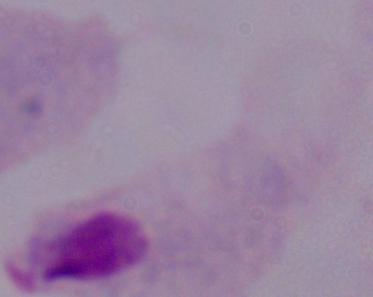

Micrograph. Captured at 1000x magnification. A trichomonad is shown.